Comment on the morphology of the red blood cells.
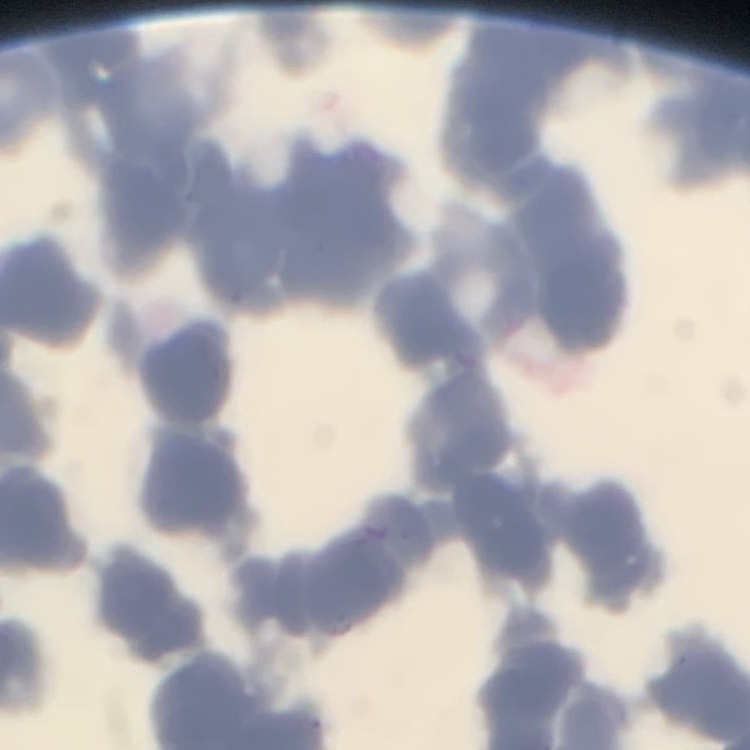

Rouleaux formation.

Square crop of a larger photomicrograph. Stained with either Field's or Giemsa. Thin blood smear.